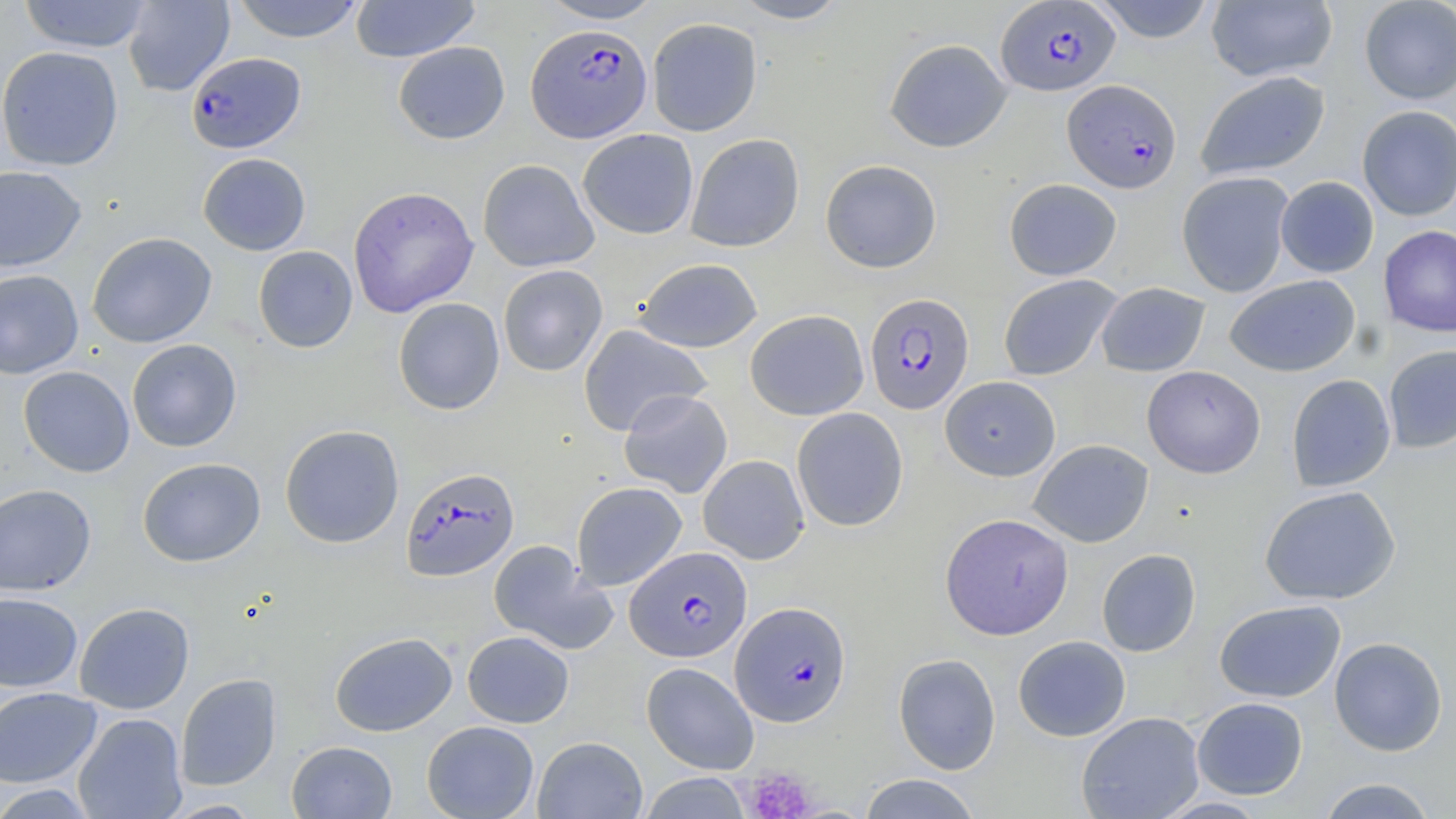
Summary:
  - Coordinate format: approximate bounding boxes as (x1,y1)-(x2,y2) corner pairs in pixels
  - Uninfected red blood cell locations: (18,0)-(154,53), (123,0)-(235,97), (231,0)-(365,43), (351,0)-(480,62), (538,0)-(665,24), (730,0)-(851,24), (1090,0)-(1218,43), (1206,0)-(1338,83), (1358,0)-(1456,105), (646,17)-(762,136), (885,38)-(1012,153), (393,42)-(510,144), (0,46)-(124,171), (1195,70)-(1330,181), (1357,105)-(1456,221), (578,129)-(699,239), (686,133)-(805,252), (197,152)-(311,256), (477,159)-(599,272), (820,159)-(942,273), (0,165)-(87,272), (1176,171)-(1295,298), (1275,176)-(1379,278), (1004,178)-(1122,281), (347,186)-(479,317), (1378,225)-(1456,338), (87,232)-(217,348), (253,245)-(358,353), (634,258)-(762,352), (497,264)-(608,376), (0,269)-(84,379), (998,274)-(1122,380), (1224,275)-(1360,377), (1096,282)-(1210,377), (393,298)-(505,415), (744,309)-(869,420), (578,324)-(712,436), (126,339)-(242,452), (1383,344)-(1456,453), (18,365)-(135,477), (1142,365)-(1266,478), (1286,374)-(1396,492), (940,375)-(1061,480), (619,389)-(732,498), (791,407)-(908,532), (279,424)-(404,548), (1028,439)-(1154,548), (698,455)-(809,564), (137,457)-(266,567), (571,481)-(687,590), (0,483)-(97,596), (1259,485)-(1401,605), (940,512)-(1074,639), (488,540)-(616,653), (1097,548)-(1201,657), (0,592)-(83,693), (1214,599)-(1346,703), (74,602)-(195,715), (330,631)-(457,736), (462,631)-(574,728), (1013,635)-(1131,741), (1329,636)-(1448,756), (893,653)-(1001,775), (641,661)-(759,774), (176,673)-(282,790), (0,686)-(102,788), (1192,697)-(1308,800), (1076,711)-(1205,818), (73,712)-(188,819), (422,720)-(539,819), (533,736)-(647,819), (286,740)-(397,818), (638,771)-(751,818), (858,774)-(982,818), (1316,777)-(1439,818), (0,783)-(99,818), (1154,796)-(1272,818), (160,798)-(265,818)
  - Plasmodium falciparum-infected red blood cell locations: (995,1)-(1120,96), (526,24)-(652,142), (186,51)-(306,153), (1063,79)-(1181,193), (865,292)-(974,414), (400,467)-(519,581), (625,546)-(751,662), (731,601)-(851,726)
  - Platelet locations: (740,765)-(818,819)
  - Slide-level diagnosis: Plasmodium falciparum
  - Modality: optical microscopy
  - Preparation: thin blood smear
  - Image size: 1456×819 pixels
  - Stain: May-Grünwald-Giemsa
  - Field of view: one of a larger specimen
  - Magnification: 1000x